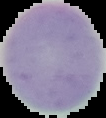 Malaria status: uninfected. Image is 106×118 pixels. Cell region segmented out of the field of view; the surrounding area is masked to black. From a thin blood film.